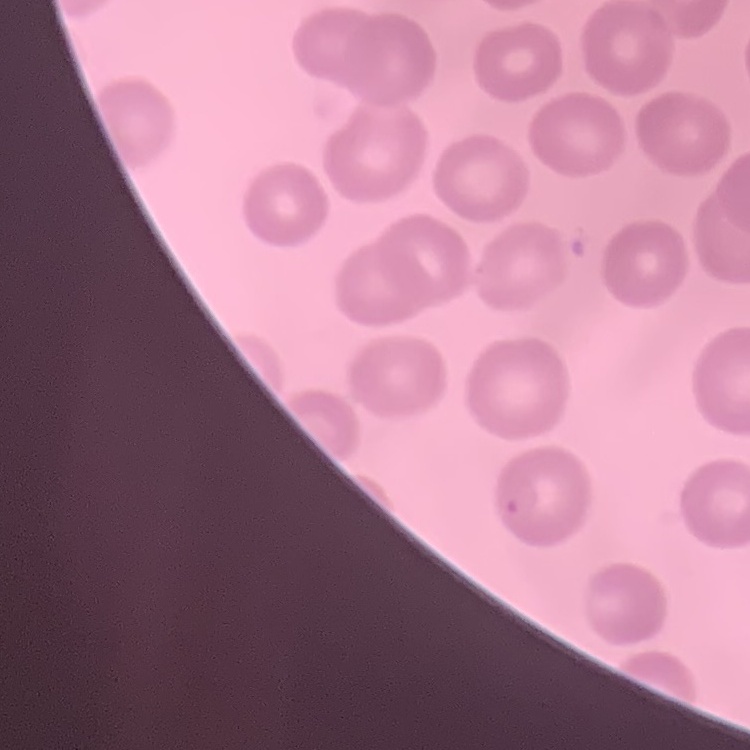

red_blood_cell_morphology: no rouleaux formation
stain: Field's or Giemsa
preparation: thin peripheral smear
image_type: one tile cut from a larger photomicrograph